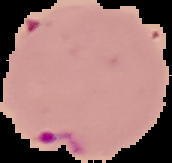

{
  "preparation": "thin blood film",
  "image_type": "cell region segmented out of the field of view; surrounding area masked to black",
  "result": "Plasmodium parasites identified",
  "image_size": "172×163 pixels"
}